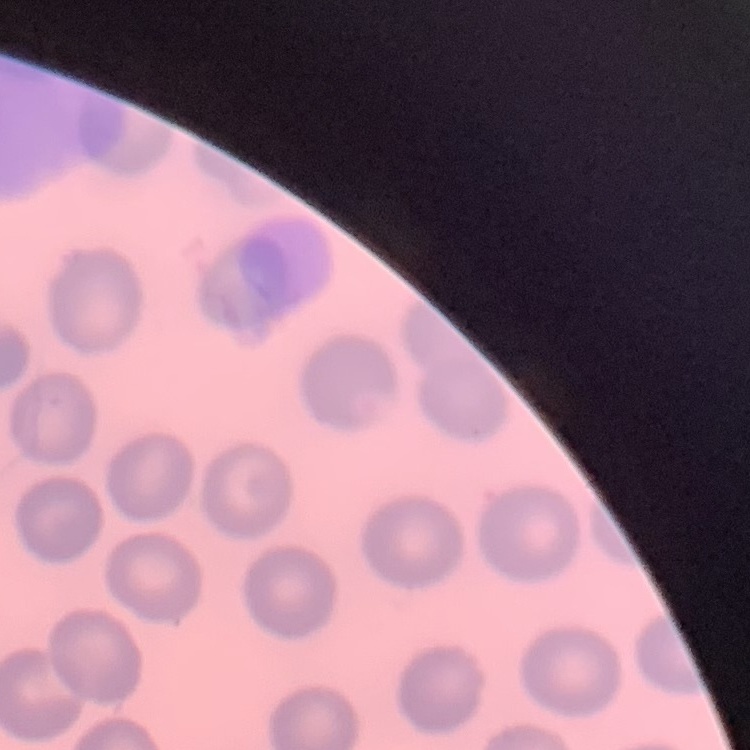
erythrocyte morphology = no rouleaux formation
preparation = thin blood film
image type = one tile cut from a larger photomicrograph
stain = Field's or Giemsa